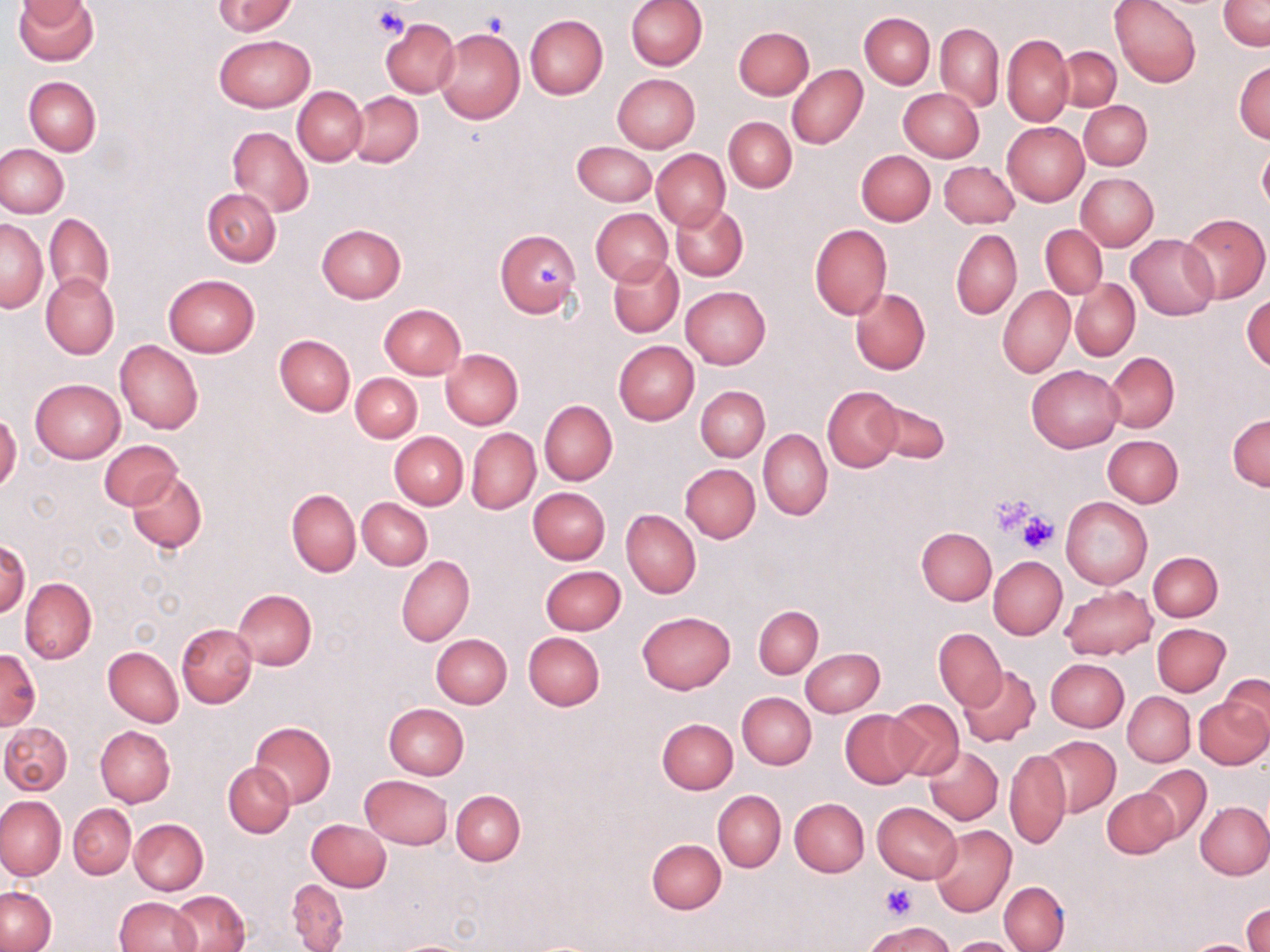

Approximate bounding boxes as named x1/y1/x2/y2 corners in pixels. Uninfected red blood cell locations: (x1=14, y1=0, x2=99, y2=64), (x1=16, y1=0, x2=93, y2=26), (x1=213, y1=0, x2=298, y2=36), (x1=625, y1=0, x2=706, y2=71), (x1=1110, y1=0, x2=1200, y2=88), (x1=1219, y1=0, x2=1269, y2=51), (x1=860, y1=12, x2=934, y2=89), (x1=525, y1=15, x2=608, y2=99), (x1=380, y1=18, x2=459, y2=97), (x1=936, y1=23, x2=1002, y2=112), (x1=734, y1=26, x2=814, y2=99), (x1=434, y1=27, x2=524, y2=123), (x1=215, y1=34, x2=314, y2=112), (x1=1002, y1=34, x2=1074, y2=127), (x1=1057, y1=45, x2=1121, y2=113), (x1=1233, y1=62, x2=1270, y2=142), (x1=786, y1=64, x2=868, y2=149), (x1=611, y1=74, x2=699, y2=153), (x1=24, y1=76, x2=101, y2=155), (x1=293, y1=87, x2=366, y2=165), (x1=899, y1=88, x2=984, y2=161), (x1=348, y1=91, x2=422, y2=167), (x1=1078, y1=100, x2=1152, y2=170), (x1=724, y1=117, x2=796, y2=191), (x1=1002, y1=121, x2=1089, y2=206), (x1=227, y1=126, x2=313, y2=216), (x1=572, y1=141, x2=656, y2=206), (x1=0, y1=144, x2=68, y2=218), (x1=1258, y1=144, x2=1270, y2=213), (x1=651, y1=148, x2=729, y2=231), (x1=856, y1=150, x2=935, y2=225), (x1=940, y1=161, x2=1019, y2=228), (x1=1076, y1=172, x2=1158, y2=250), (x1=202, y1=188, x2=281, y2=267), (x1=671, y1=204, x2=748, y2=281), (x1=591, y1=209, x2=672, y2=285), (x1=44, y1=212, x2=114, y2=299), (x1=1181, y1=213, x2=1269, y2=303), (x1=1, y1=219, x2=47, y2=311), (x1=316, y1=224, x2=406, y2=303), (x1=810, y1=224, x2=892, y2=320), (x1=1041, y1=224, x2=1106, y2=298), (x1=495, y1=229, x2=581, y2=318), (x1=951, y1=229, x2=1022, y2=319), (x1=1125, y1=234, x2=1219, y2=321), (x1=608, y1=256, x2=683, y2=337), (x1=41, y1=272, x2=118, y2=359), (x1=163, y1=274, x2=258, y2=357), (x1=1071, y1=279, x2=1140, y2=361), (x1=680, y1=285, x2=771, y2=370), (x1=998, y1=286, x2=1074, y2=377), (x1=850, y1=288, x2=930, y2=374), (x1=1243, y1=293, x2=1270, y2=371), (x1=378, y1=303, x2=467, y2=380), (x1=273, y1=335, x2=355, y2=417), (x1=116, y1=339, x2=203, y2=434), (x1=614, y1=341, x2=699, y2=424), (x1=439, y1=348, x2=523, y2=430), (x1=1105, y1=352, x2=1179, y2=433), (x1=1026, y1=364, x2=1123, y2=452), (x1=350, y1=372, x2=422, y2=442), (x1=30, y1=378, x2=125, y2=464), (x1=696, y1=385, x2=770, y2=461), (x1=822, y1=386, x2=902, y2=472), (x1=540, y1=399, x2=617, y2=485), (x1=871, y1=400, x2=949, y2=464), (x1=0, y1=413, x2=21, y2=494), (x1=1228, y1=413, x2=1269, y2=491), (x1=467, y1=428, x2=540, y2=514), (x1=758, y1=429, x2=832, y2=519), (x1=389, y1=432, x2=467, y2=509), (x1=1102, y1=435, x2=1183, y2=507), (x1=100, y1=441, x2=181, y2=509), (x1=679, y1=463, x2=760, y2=543), (x1=128, y1=469, x2=207, y2=553), (x1=529, y1=488, x2=610, y2=563), (x1=287, y1=489, x2=360, y2=577), (x1=1060, y1=497, x2=1153, y2=589), (x1=357, y1=498, x2=431, y2=569), (x1=621, y1=510, x2=701, y2=599), (x1=916, y1=527, x2=997, y2=604), (x1=1, y1=539, x2=30, y2=618), (x1=1148, y1=550, x2=1222, y2=622), (x1=397, y1=555, x2=474, y2=645), (x1=988, y1=556, x2=1067, y2=640), (x1=541, y1=565, x2=625, y2=634), (x1=20, y1=578, x2=97, y2=665), (x1=1059, y1=584, x2=1156, y2=660), (x1=232, y1=589, x2=317, y2=670), (x1=753, y1=605, x2=823, y2=678), (x1=637, y1=611, x2=734, y2=693), (x1=177, y1=623, x2=257, y2=709), (x1=1152, y1=623, x2=1230, y2=696), (x1=934, y1=628, x2=1006, y2=711), (x1=523, y1=632, x2=605, y2=711), (x1=431, y1=634, x2=512, y2=709), (x1=104, y1=647, x2=183, y2=727), (x1=801, y1=647, x2=885, y2=717), (x1=1, y1=649, x2=39, y2=729), (x1=1045, y1=658, x2=1129, y2=731), (x1=957, y1=664, x2=1041, y2=749), (x1=1222, y1=675, x2=1270, y2=744), (x1=737, y1=692, x2=816, y2=768), (x1=1123, y1=692, x2=1194, y2=766), (x1=1195, y1=696, x2=1270, y2=769), (x1=885, y1=699, x2=963, y2=780), (x1=383, y1=703, x2=469, y2=780), (x1=840, y1=710, x2=919, y2=788), (x1=656, y1=718, x2=738, y2=794), (x1=249, y1=721, x2=336, y2=807), (x1=1, y1=722, x2=73, y2=794), (x1=96, y1=725, x2=175, y2=808), (x1=1040, y1=736, x2=1120, y2=817), (x1=923, y1=745, x2=1003, y2=825), (x1=1005, y1=749, x2=1071, y2=850), (x1=224, y1=761, x2=295, y2=838), (x1=1137, y1=765, x2=1212, y2=844), (x1=360, y1=775, x2=454, y2=849), (x1=1102, y1=788, x2=1176, y2=859), (x1=713, y1=790, x2=786, y2=872), (x1=451, y1=791, x2=525, y2=866), (x1=0, y1=795, x2=66, y2=880), (x1=789, y1=798, x2=869, y2=876), (x1=1196, y1=801, x2=1270, y2=879), (x1=873, y1=802, x2=961, y2=883), (x1=68, y1=803, x2=135, y2=879), (x1=307, y1=818, x2=392, y2=891), (x1=130, y1=819, x2=208, y2=895), (x1=930, y1=825, x2=1015, y2=916), (x1=646, y1=839, x2=726, y2=914), (x1=287, y1=880, x2=349, y2=951), (x1=999, y1=881, x2=1070, y2=951), (x1=1, y1=888, x2=56, y2=951), (x1=170, y1=890, x2=249, y2=952), (x1=114, y1=896, x2=200, y2=952), (x1=1244, y1=906, x2=1269, y2=952), (x1=866, y1=920, x2=953, y2=952), (x1=946, y1=936, x2=1023, y2=951). Platelet locations: (x1=373, y1=5, x2=411, y2=39), (x1=533, y1=257, x2=566, y2=293), (x1=990, y1=493, x2=1037, y2=535), (x1=1017, y1=513, x2=1058, y2=554), (x1=881, y1=885, x2=917, y2=918). Slide-level diagnosis: negative for blood parasites. One field of a larger specimen. Image is 1270×952 pixels. Thin blood smear. Optical microscopy. 1000x magnification. May-Grünwald-Giemsa-stained preparation.